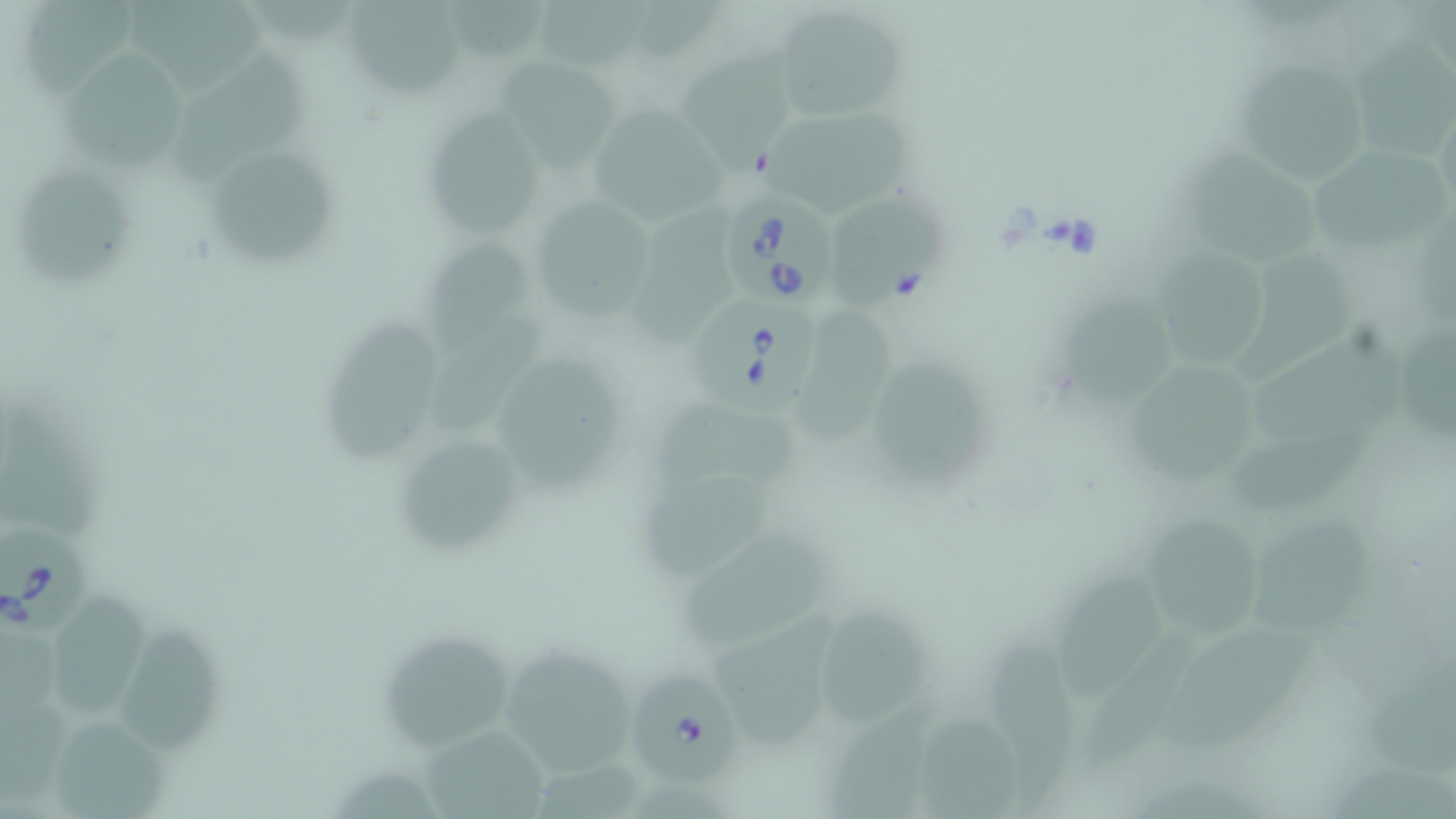
Summary:
  - Coordinate format: approximate bounding boxes as (x1,y1)-(x2,y2) corner pairs in pixels
  - Babesia divergens-infected red blood cell locations: (725,190)-(839,305), (696,294)-(825,421), (0,521)-(91,637), (629,667)-(743,789)
  - Uninfected red blood cell locations: (29,0)-(148,97), (123,0)-(280,93), (341,0)-(466,100), (452,0)-(553,64), (541,0)-(654,69), (640,0)-(726,64), (770,5)-(907,126), (1362,35)-(1447,166), (681,43)-(797,173), (56,50)-(191,170), (175,50)-(318,183), (501,56)-(623,176), (1232,57)-(1372,191), (590,100)-(737,220), (421,106)-(545,236), (757,108)-(920,220), (1187,141)-(1325,265), (1306,145)-(1448,257), (213,149)-(337,262), (18,161)-(139,288), (830,193)-(951,316), (634,196)-(746,350), (530,202)-(654,313), (416,235)-(539,349), (1163,250)-(1275,366), (1245,252)-(1359,380), (1063,289)-(1179,407), (804,307)-(903,443), (435,310)-(545,434), (325,313)-(440,464), (1404,316)-(1447,434), (1257,336)-(1410,451), (500,355)-(624,498), (875,355)-(988,489), (1132,364)-(1261,486), (647,391)-(805,494), (0,396)-(97,536), (387,428)-(535,558), (1232,434)-(1375,509), (640,470)-(775,581), (1142,505)-(1262,642), (1259,519)-(1382,640), (685,535)-(834,652), (1057,570)-(1170,692), (54,591)-(155,719), (820,605)-(930,730), (710,612)-(839,754), (117,623)-(224,755), (1080,623)-(1203,773), (1166,623)-(1315,754), (374,626)-(522,750), (991,630)-(1083,811), (1,631)-(65,720), (496,641)-(641,781), (1358,666)-(1456,778), (829,691)-(934,819), (1,701)-(69,807), (921,703)-(1016,819), (53,719)-(168,819), (422,719)-(547,819), (1329,750)-(1456,819)
  - Slide-level diagnosis: Babesia divergens
  - Preparation: thin blood smear
  - Magnification: 1000x
  - Modality: light microscopy
  - Stain: May-Grünwald-Giemsa
  - Field of view: single
  - Image size: 1456×819 pixels